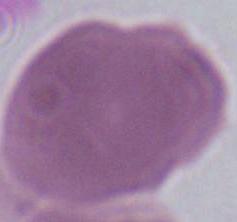

Summary:
  - Identification: red blood cell
  - Magnification: 1000x
  - Modality: micrograph